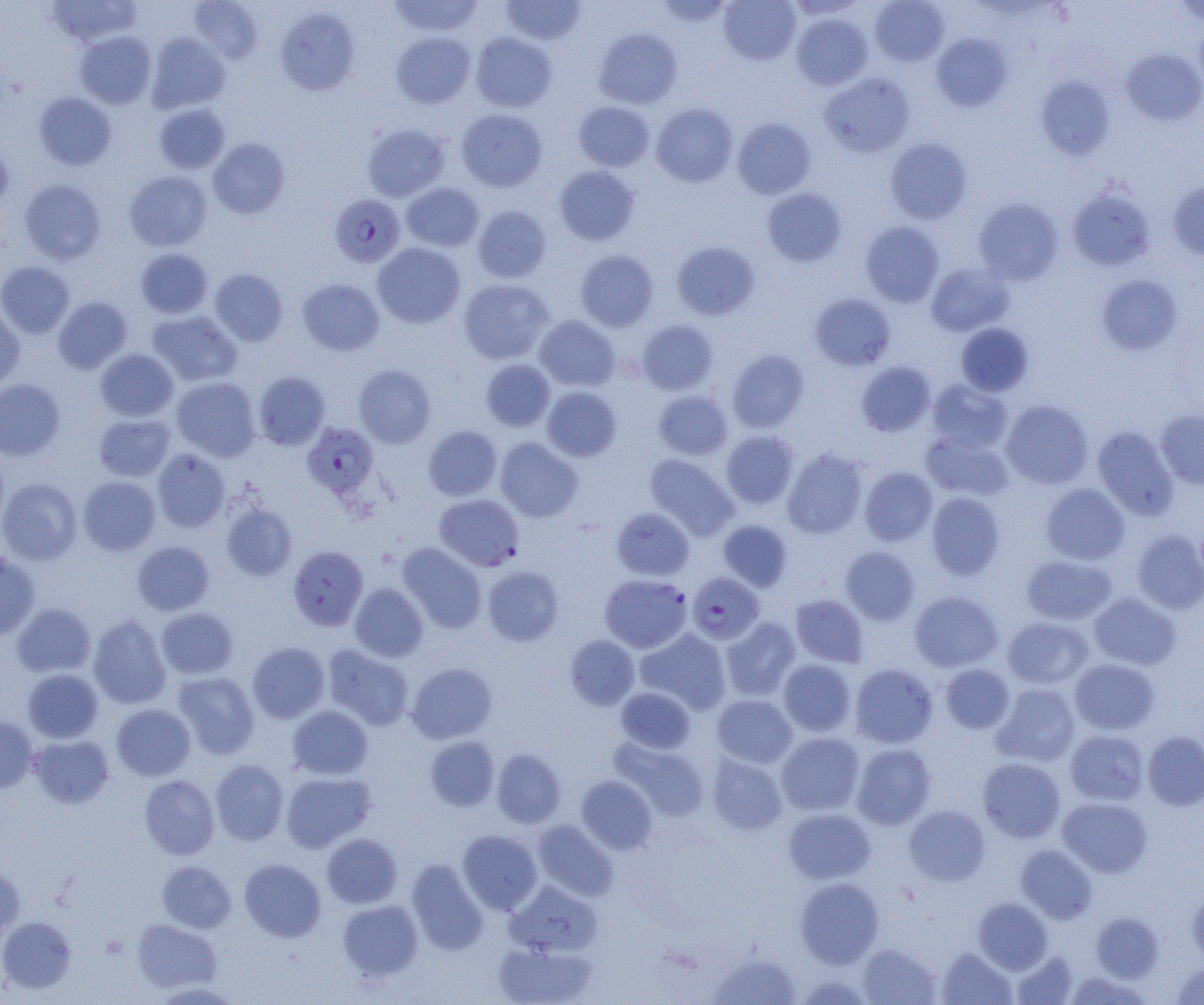
slide-level diagnosis = Plasmodium falciparum
preparation = thin blood film
image size = 1204×1005 pixels
uninfected red blood cell locations (subset) = approximate bounding boxes as (x1, y1, x2, y2) in pixels: (46, 0, 142, 47), (189, 0, 263, 63), (387, 0, 485, 37), (500, 0, 586, 46), (653, 0, 735, 28), (718, 0, 801, 65), (869, 1, 950, 66), (1173, 1, 1204, 26), (275, 6, 360, 96), (791, 13, 873, 90), (1195, 23, 1204, 97), (593, 27, 683, 109), (74, 30, 157, 109), (391, 31, 476, 109), (470, 31, 557, 113), (146, 32, 230, 114), (931, 33, 1012, 112), (1121, 48, 1204, 125), (819, 72, 915, 157), (1035, 75, 1116, 160), (33, 92, 116, 170), (573, 101, 655, 172), (154, 103, 230, 173), (651, 103, 738, 187), (456, 108, 547, 192), (732, 118, 817, 199), (362, 124, 450, 202), (208, 138, 290, 218), (885, 138, 972, 224), (0, 142, 13, 216), (554, 165, 639, 245), (124, 170, 212, 251), (19, 179, 106, 264), (1168, 180, 1204, 261), (401, 182, 484, 252), (762, 187, 847, 267), (1066, 188, 1156, 272), (973, 197, 1064, 285), (472, 205, 551, 283), (861, 221, 944, 307), (671, 241, 760, 321), (372, 242, 466, 328), (136, 248, 213, 319), (575, 250, 659, 331), (0, 261, 75, 338), (926, 263, 1015, 336), (210, 268, 288, 346), (1096, 274, 1183, 356), (297, 278, 384, 356), (458, 278, 554, 365), (810, 293, 896, 371), (53, 296, 132, 374), (0, 307, 24, 392), (147, 310, 242, 388), (534, 315, 620, 391), (636, 319, 718, 395), (955, 323, 1034, 397), (95, 348, 178, 422), (727, 349, 809, 432), (481, 359, 555, 431), (856, 361, 936, 437), (354, 364, 436, 448), (253, 372, 330, 450), (171, 376, 261, 461), (0, 379, 65, 460), (926, 379, 1013, 453), (542, 386, 621, 462), (653, 390, 732, 460), (1001, 399, 1093, 489), (1155, 408, 1204, 489), (93, 414, 175, 482), (423, 425, 502, 501), (1092, 425, 1180, 520), (921, 430, 1013, 501), (721, 431, 799, 509), (495, 437, 583, 522), (152, 448, 231, 533), (782, 448, 868, 539), (645, 453, 738, 540), (860, 467, 937, 546), (78, 476, 161, 555), (0, 478, 82, 565), (1040, 483, 1130, 565), (926, 492, 1005, 580), (221, 503, 298, 581), (611, 507, 694, 580), (718, 520, 793, 591), (1132, 530, 1204, 614), (132, 541, 214, 615), (397, 543, 487, 633), (840, 546, 920, 625), (0, 553, 40, 639), (1021, 554, 1118, 625), (482, 565, 564, 646), (350, 583, 429, 662), (909, 591, 1003, 672), (1088, 592, 1181, 670), (790, 594, 869, 668), (11, 602, 96, 678), (156, 607, 238, 679), (88, 615, 172, 709), (721, 616, 800, 701), (1003, 616, 1093, 689), (635, 628, 730, 714), (565, 635, 639, 710), (247, 642, 329, 723), (323, 645, 414, 731), (778, 659, 856, 736), (1070, 659, 1160, 734), (407, 663, 497, 744), (850, 663, 937, 748), (940, 664, 1015, 733), (22, 668, 103, 743), (173, 671, 260, 759), (992, 683, 1080, 767), (615, 687, 695, 753), (712, 694, 797, 768), (111, 703, 195, 781), (287, 705, 372, 779), (0, 715, 39, 792), (1065, 729, 1149, 805), (1142, 730, 1204, 811), (776, 732, 865, 816), (28, 735, 114, 808), (424, 736, 499, 812), (613, 739, 710, 822), (852, 743, 936, 829), (491, 749, 565, 828), (707, 753, 788, 835), (977, 757, 1065, 843), (210, 759, 288, 845), (280, 771, 376, 852), (139, 775, 219, 859), (576, 775, 657, 855), (1057, 797, 1152, 877), (904, 805, 990, 886), (783, 808, 876, 884), (532, 819, 618, 901), (457, 829, 542, 915), (321, 833, 402, 908), (1016, 845, 1097, 923), (239, 859, 326, 941), (407, 859, 488, 955), (157, 860, 236, 933), (0, 864, 25, 942), (795, 877, 883, 968), (505, 881, 602, 957), (1186, 883, 1204, 963), (973, 897, 1052, 973), (338, 899, 423, 980), (1091, 912, 1163, 983), (0, 916, 76, 993), (132, 919, 222, 993), (493, 941, 597, 1005), (857, 942, 940, 1005), (937, 947, 1017, 1004), (1011, 951, 1079, 1004), (708, 953, 801, 1004), (1171, 961, 1204, 1004), (1064, 971, 1152, 1004), (150, 981, 242, 1004)
field of view = single
magnification = 1000x
Plasmodium falciparum-infected red blood cell locations (subset) = approximate bounding boxes as (x1, y1, x2, y2) in pixels: (329, 194, 405, 267), (302, 422, 378, 498), (288, 545, 368, 631), (687, 572, 765, 644), (599, 574, 692, 653)
modality = optical microscopy